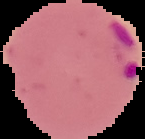
result: malaria parasites detected
image_type: cell region segmented out of the field of view; surrounding area masked to black
preparation: thin blood smear
image_size: 145×139 pixels